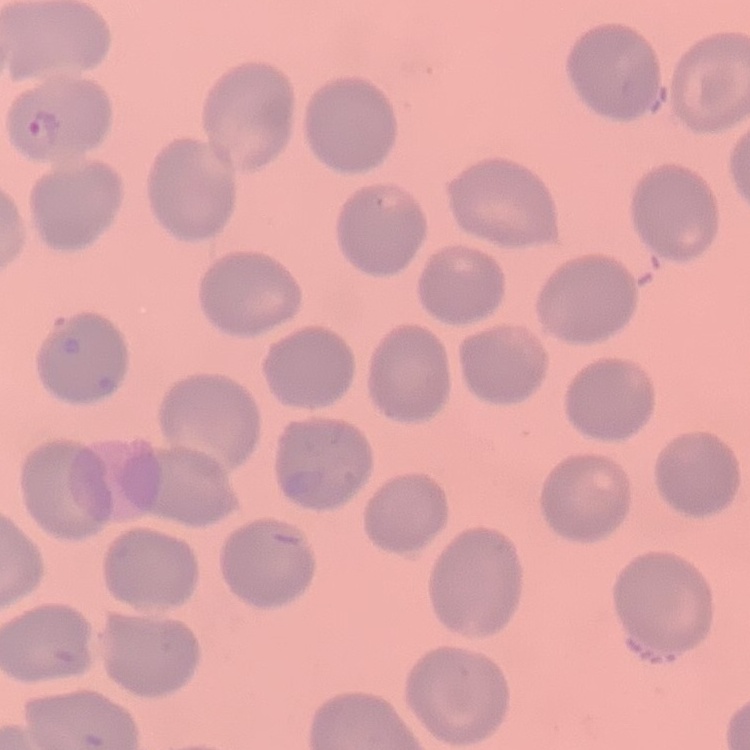
erythrocyte morphology = no rouleaux formation
preparation = thin blood film
image type = one tile cut from a larger photomicrograph
stain = Field's or Giemsa